Identify the parasite.
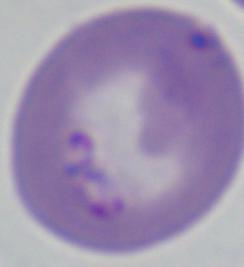
Babesia.

{
  "modality": "photomicrograph",
  "magnification": "1000x"
}